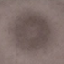 Malaria status: uninfected. Automatically extracted cell patch, resized to 64 × 64 pixels. Acquired by smartphone through the microscope eyepiece. Thin blood smear. Giemsa stain.